Point out each Plasmodium parasite.
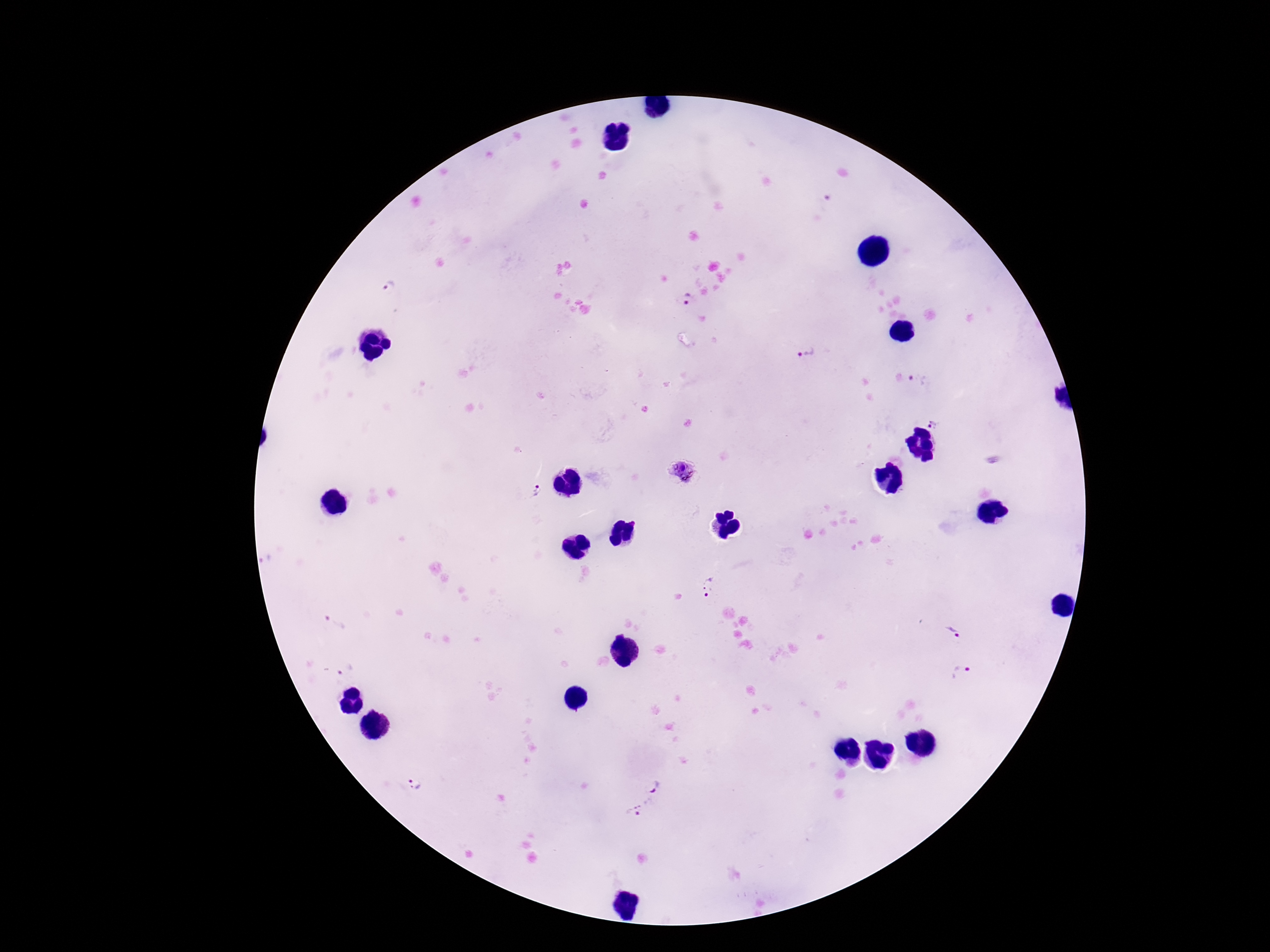

Approximate object centers, in pixels from the top-left corner.
Plasmodium parasites: (x=391, y=286), (x=688, y=300), (x=806, y=353), (x=918, y=380), (x=937, y=422), (x=681, y=470), (x=534, y=491), (x=709, y=587), (x=336, y=622), (x=958, y=630), (x=345, y=670), (x=964, y=675), (x=414, y=786), (x=657, y=788), (x=638, y=810).

{
  "magnification": "100x",
  "image_size": "1270×952 pixels",
  "preparation": "thick peripheral-blood smear",
  "patient_malaria_status": "positive",
  "field_of_view": "one from this slide",
  "capture": "smartphone camera through the microscope eyepiece",
  "stain": "Giemsa"
}